Mark where platelets are.
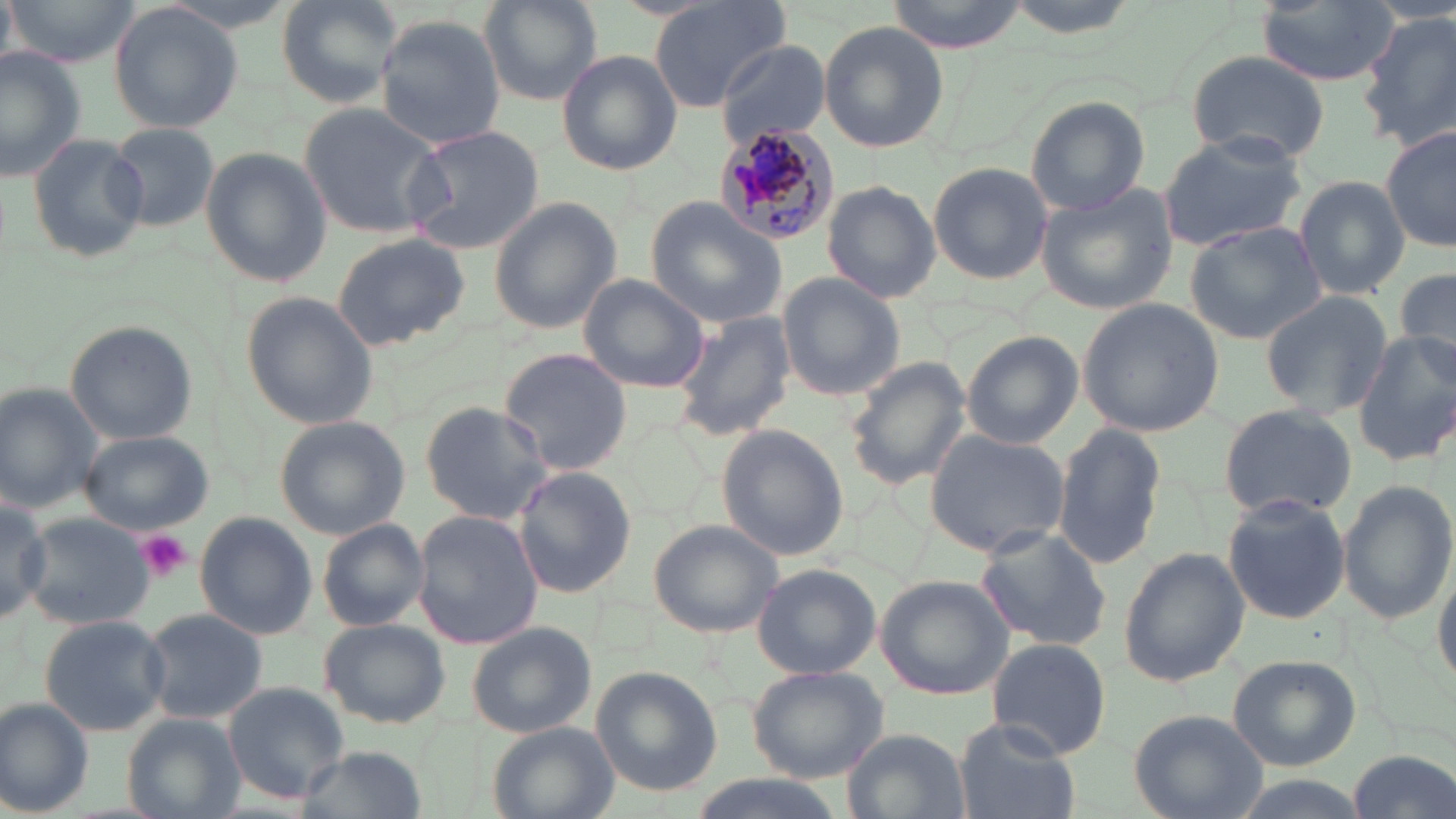

Approximate bounding boxes as named x1/y1/x2/y2 corners in pixels.
Platelets: (x1=132, y1=530, x2=193, y2=584).

Summary:
  - Plasmodium malariae-infected red blood cell locations: (x1=714, y1=123, x2=844, y2=246)
  - Uninfected red blood cell locations: (x1=0, y1=0, x2=16, y2=69), (x1=3, y1=0, x2=144, y2=68), (x1=274, y1=0, x2=405, y2=105), (x1=479, y1=0, x2=603, y2=106), (x1=649, y1=0, x2=790, y2=112), (x1=885, y1=0, x2=1030, y2=49), (x1=1256, y1=0, x2=1398, y2=86), (x1=109, y1=2, x2=242, y2=133), (x1=1358, y1=10, x2=1456, y2=150), (x1=375, y1=14, x2=508, y2=147), (x1=818, y1=22, x2=949, y2=154), (x1=717, y1=41, x2=833, y2=148), (x1=0, y1=47, x2=87, y2=180), (x1=1184, y1=49, x2=1332, y2=165), (x1=558, y1=50, x2=682, y2=176), (x1=1026, y1=97, x2=1151, y2=217), (x1=297, y1=101, x2=449, y2=240), (x1=106, y1=122, x2=220, y2=233), (x1=400, y1=124, x2=544, y2=256), (x1=1383, y1=125, x2=1456, y2=254), (x1=1157, y1=131, x2=1308, y2=253), (x1=28, y1=134, x2=149, y2=263), (x1=199, y1=147, x2=332, y2=289), (x1=928, y1=162, x2=1053, y2=284), (x1=1295, y1=175, x2=1411, y2=298), (x1=822, y1=181, x2=942, y2=302), (x1=1036, y1=184, x2=1179, y2=316), (x1=489, y1=198, x2=621, y2=335), (x1=647, y1=200, x2=789, y2=329), (x1=1186, y1=221, x2=1327, y2=345), (x1=331, y1=231, x2=470, y2=350), (x1=1393, y1=263, x2=1456, y2=376), (x1=579, y1=273, x2=712, y2=394), (x1=777, y1=273, x2=905, y2=400), (x1=1259, y1=289, x2=1392, y2=421), (x1=240, y1=293, x2=379, y2=430), (x1=1079, y1=299, x2=1227, y2=436), (x1=669, y1=309, x2=796, y2=442), (x1=65, y1=320, x2=198, y2=446), (x1=961, y1=331, x2=1086, y2=450), (x1=1351, y1=332, x2=1456, y2=466), (x1=498, y1=347, x2=631, y2=475), (x1=842, y1=355, x2=973, y2=491), (x1=0, y1=383, x2=103, y2=512), (x1=420, y1=402, x2=554, y2=527), (x1=1217, y1=404, x2=1357, y2=522), (x1=275, y1=418, x2=409, y2=539), (x1=1054, y1=423, x2=1166, y2=571), (x1=715, y1=424, x2=850, y2=561), (x1=924, y1=428, x2=1071, y2=557), (x1=79, y1=430, x2=216, y2=533), (x1=514, y1=467, x2=635, y2=598), (x1=1339, y1=479, x2=1456, y2=626), (x1=0, y1=492, x2=49, y2=630), (x1=1222, y1=495, x2=1351, y2=625), (x1=412, y1=511, x2=544, y2=651), (x1=20, y1=512, x2=156, y2=630), (x1=195, y1=512, x2=320, y2=639), (x1=317, y1=519, x2=432, y2=631), (x1=649, y1=519, x2=786, y2=638), (x1=973, y1=525, x2=1111, y2=651), (x1=1118, y1=547, x2=1251, y2=689), (x1=1433, y1=551, x2=1456, y2=694), (x1=751, y1=563, x2=882, y2=679), (x1=875, y1=575, x2=1014, y2=700), (x1=141, y1=608, x2=267, y2=724), (x1=38, y1=614, x2=169, y2=735), (x1=321, y1=619, x2=449, y2=728), (x1=467, y1=623, x2=595, y2=737), (x1=986, y1=637, x2=1110, y2=759), (x1=1227, y1=653, x2=1363, y2=770), (x1=589, y1=665, x2=723, y2=797), (x1=748, y1=666, x2=889, y2=783), (x1=221, y1=680, x2=350, y2=805), (x1=0, y1=696, x2=94, y2=819), (x1=1128, y1=709, x2=1266, y2=818), (x1=120, y1=714, x2=245, y2=819), (x1=953, y1=719, x2=1081, y2=819), (x1=486, y1=724, x2=619, y2=819), (x1=843, y1=728, x2=968, y2=819), (x1=294, y1=746, x2=426, y2=819), (x1=1350, y1=749, x2=1452, y2=819)
  - Slide-level diagnosis: Plasmodium malariae
  - Field of view: one of a larger specimen
  - Magnification: 1000x
  - Image size: 1456×819 pixels
  - Modality: light microscopy
  - Stain: May-Grünwald-Giemsa
  - Preparation: thin blood film